Assess this cell for malaria.
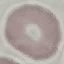
Uninfected.

Cell patch, automatically extracted from a larger field of view and resized to 64 × 64 pixels. Acquired by smartphone through the microscope eyepiece. Thin blood smear. Giemsa-stained preparation.